Name the blood parasite species.
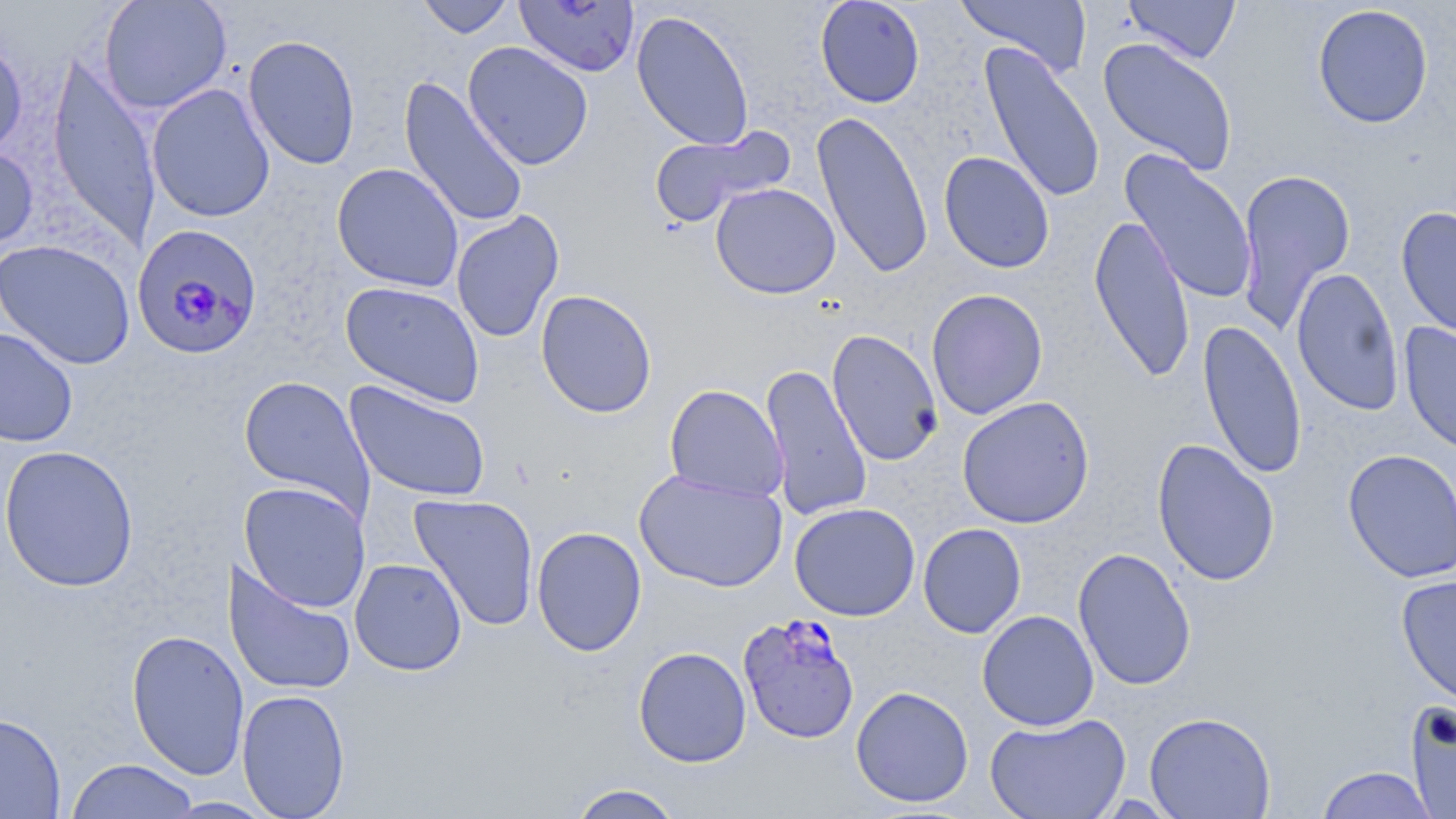

Plasmodium falciparum.

Summary:
  - Coordinate format: approximate bounding boxes as [x1, y1, x2, y2] in pixels
  - Plasmodium falciparum-infected red blood cell locations: [131, 224, 263, 361], [738, 613, 860, 745]
  - Uninfected red blood cell locations: [98, 0, 232, 114], [416, 0, 515, 38], [815, 0, 925, 108], [955, 0, 1093, 79], [1122, 0, 1241, 64], [514, 1, 640, 77], [1312, 4, 1434, 129], [631, 9, 755, 151], [0, 30, 29, 160], [243, 34, 361, 170], [1097, 37, 1238, 176], [462, 42, 594, 170], [978, 42, 1106, 205], [47, 52, 161, 252], [398, 76, 529, 230], [147, 83, 275, 223], [812, 110, 934, 279], [648, 125, 794, 230], [0, 145, 39, 253], [1120, 150, 1259, 305], [938, 151, 1055, 273], [331, 163, 464, 292], [1234, 167, 1357, 334], [710, 183, 841, 299], [1396, 206, 1456, 343], [450, 210, 565, 343], [1088, 212, 1196, 384], [0, 239, 136, 369], [1291, 267, 1404, 416], [341, 281, 486, 408], [926, 288, 1048, 419], [535, 289, 658, 418], [1197, 319, 1307, 479], [1399, 322, 1456, 456], [0, 325, 79, 447], [826, 329, 944, 467], [759, 362, 873, 522], [238, 375, 375, 516], [344, 380, 491, 503], [664, 384, 789, 503], [957, 396, 1095, 529], [1151, 438, 1281, 587], [0, 444, 139, 593], [1342, 448, 1456, 583], [634, 469, 787, 593], [238, 481, 372, 613], [409, 493, 540, 631], [789, 502, 921, 621], [917, 523, 1026, 638], [531, 526, 647, 657], [1072, 547, 1197, 691], [223, 558, 357, 698], [349, 558, 467, 675], [1397, 575, 1456, 711], [976, 610, 1099, 731], [126, 628, 250, 781], [632, 646, 751, 768], [850, 686, 974, 807], [236, 688, 351, 818], [1405, 699, 1456, 819], [1144, 711, 1276, 818], [0, 712, 66, 818], [985, 712, 1131, 819], [65, 759, 201, 818], [1314, 765, 1439, 819], [565, 783, 686, 819], [161, 796, 279, 818]
  - Stain: May-Grünwald-Giemsa
  - Field of view: one of a larger specimen
  - Image size: 1456×819 pixels
  - Preparation: thin blood smear
  - Modality: optical microscopy
  - Magnification: 1000x